Identify the parasite.
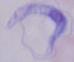

This is a trypanosome.

Micrograph. Captured at 1000x magnification.